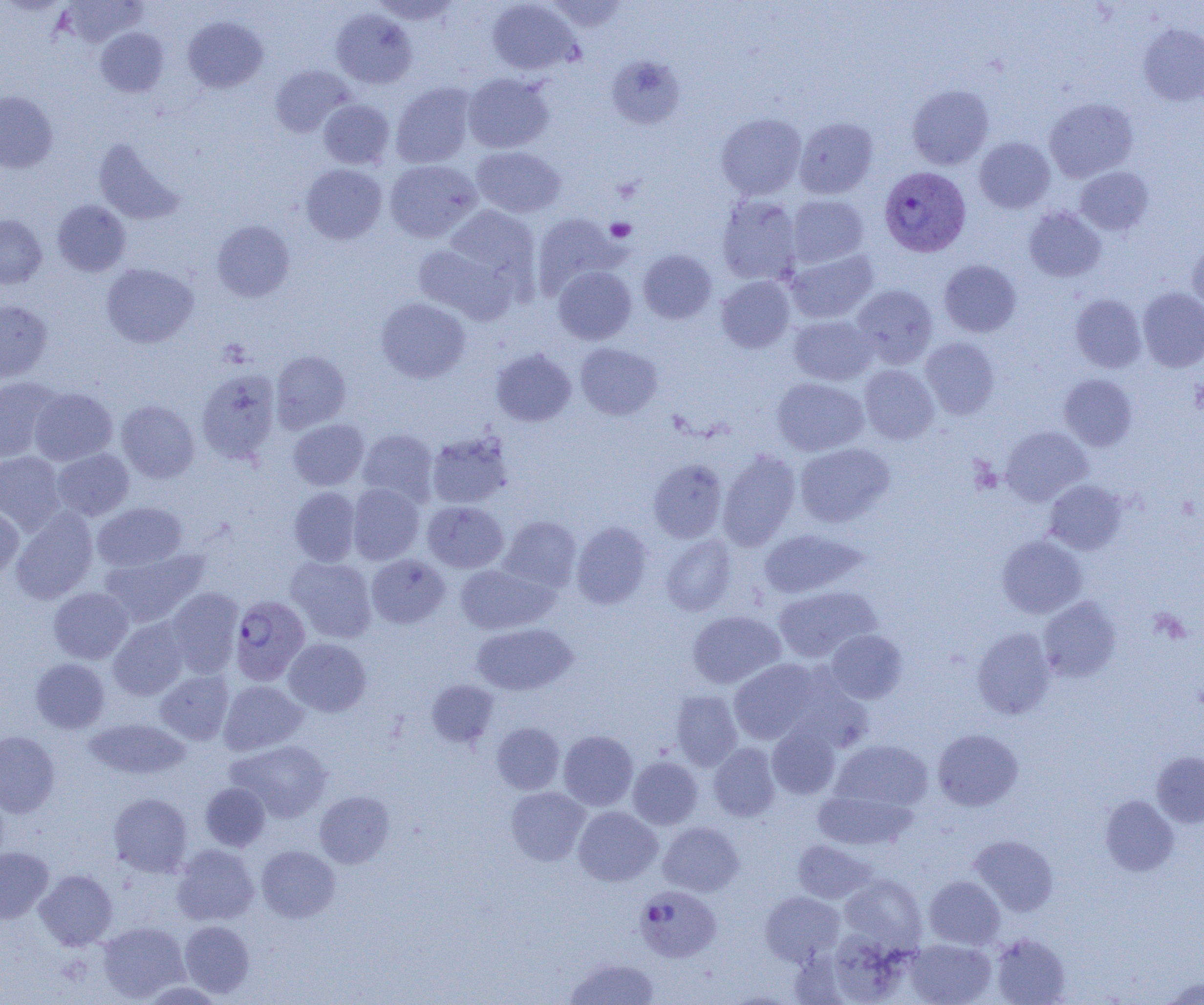

{
  "plasmodium_vivax_infected_red_blood_cell_locations": "approximate bounding boxes as [x1, y1, x2, y2] in pixels: [879, 166, 971, 257], [229, 595, 310, 686], [635, 885, 721, 962]",
  "slide_level_diagnosis": "Plasmodium vivax",
  "preparation": "thin blood film",
  "magnification": "1000x",
  "modality": "optical microscopy",
  "uninfected_red_blood_cell_locations": "approximate bounding boxes as [x1, y1, x2, y2] in pixels: [62, 0, 147, 47], [368, 0, 462, 25], [546, 0, 628, 32], [487, 1, 581, 76], [331, 7, 417, 89], [183, 16, 268, 92], [1139, 23, 1204, 105], [95, 27, 168, 97], [607, 55, 685, 129], [270, 64, 354, 138], [463, 73, 554, 153], [391, 83, 475, 168], [907, 85, 994, 170], [0, 91, 58, 173], [1044, 97, 1138, 182], [319, 99, 394, 169], [716, 113, 807, 200], [794, 117, 878, 198], [975, 137, 1055, 213], [92, 138, 184, 225], [472, 145, 565, 218], [384, 160, 481, 243], [301, 164, 387, 244], [1076, 166, 1152, 235], [717, 195, 802, 284], [787, 195, 868, 268], [52, 200, 130, 276], [443, 205, 541, 290], [1024, 207, 1106, 282], [532, 212, 623, 296], [0, 214, 47, 288], [211, 220, 294, 302], [1187, 241, 1204, 317], [414, 242, 520, 324], [637, 249, 717, 324], [785, 249, 878, 323], [939, 260, 1021, 337], [101, 263, 198, 348], [553, 266, 636, 345], [716, 276, 795, 353], [852, 284, 938, 368], [1137, 287, 1204, 372], [1071, 294, 1147, 372], [376, 297, 471, 383], [0, 299, 52, 383], [789, 315, 876, 385], [921, 337, 999, 419], [575, 343, 662, 420], [491, 348, 576, 427], [270, 349, 351, 433], [860, 365, 939, 444], [196, 368, 281, 464], [1059, 374, 1137, 451], [0, 377, 61, 462], [772, 377, 868, 456], [30, 387, 117, 465], [116, 400, 199, 483], [288, 418, 369, 490], [1001, 425, 1092, 506], [357, 428, 439, 508], [426, 430, 513, 509], [795, 443, 894, 528], [52, 448, 134, 520], [717, 450, 801, 550], [0, 451, 66, 535], [648, 459, 727, 543], [1043, 480, 1126, 555], [348, 483, 424, 565], [289, 487, 361, 566], [423, 501, 508, 573], [92, 502, 187, 571], [0, 504, 24, 579], [10, 508, 98, 603], [498, 516, 581, 592], [572, 521, 653, 609], [758, 528, 866, 599], [661, 534, 736, 616], [997, 535, 1087, 619], [99, 548, 209, 627], [366, 554, 449, 629], [286, 556, 377, 643], [455, 564, 556, 635], [773, 585, 880, 663], [48, 587, 133, 664], [164, 587, 244, 677], [1038, 597, 1121, 683], [687, 611, 786, 689], [108, 617, 189, 700], [471, 623, 577, 696], [972, 627, 1056, 719], [825, 629, 907, 703], [284, 638, 371, 716], [30, 658, 110, 733], [728, 659, 822, 744], [155, 670, 234, 745], [218, 680, 308, 755], [426, 680, 499, 747], [671, 690, 742, 771], [84, 717, 190, 780], [491, 722, 564, 794], [768, 724, 841, 799], [933, 729, 1023, 811], [559, 730, 638, 810], [0, 731, 60, 816], [227, 739, 333, 822], [830, 739, 933, 813], [709, 742, 780, 821], [1152, 751, 1204, 827], [628, 756, 703, 829], [200, 782, 270, 851], [506, 786, 591, 866], [813, 788, 917, 852], [314, 791, 395, 868], [108, 792, 192, 877], [1100, 795, 1179, 876], [573, 806, 662, 886], [658, 822, 744, 896], [969, 834, 1058, 916], [792, 839, 874, 903], [171, 844, 260, 926], [256, 845, 340, 922], [0, 847, 54, 923], [34, 869, 117, 950], [840, 874, 926, 951], [924, 876, 1005, 949], [760, 891, 844, 966], [179, 920, 254, 998], [98, 921, 189, 1002], [829, 931, 907, 1004], [990, 933, 1071, 1005], [904, 939, 996, 1005], [564, 957, 660, 1005], [1160, 977, 1204, 1004]",
  "platelet_locations": "approximate bounding boxes as [x1, y1, x2, y2] in pixels: [605, 218, 636, 242], [1188, 379, 1204, 414]",
  "field_of_view": "one of a larger specimen",
  "image_size": "1204×1005 pixels"
}